Identify the preparation type.
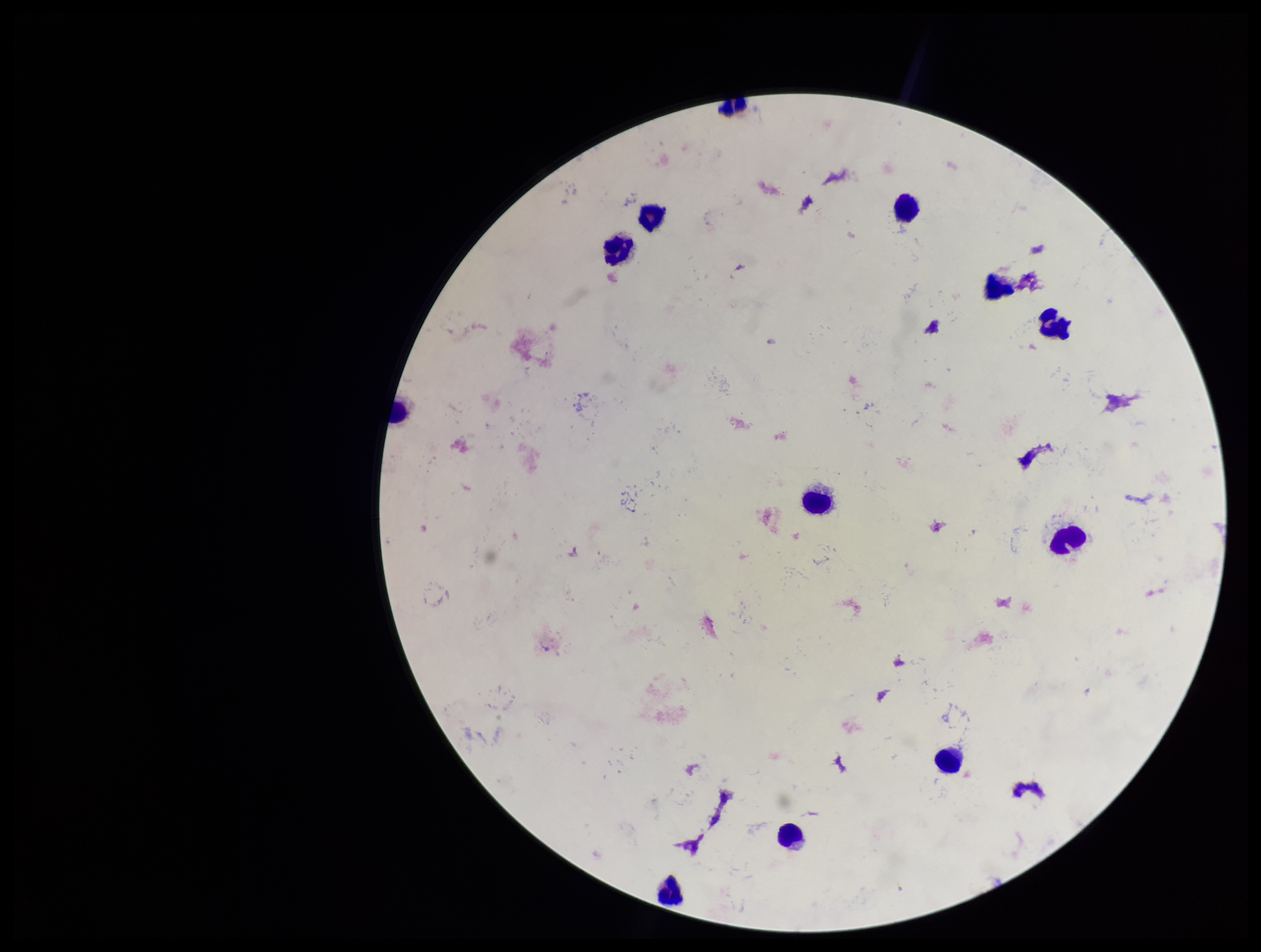

It is a thick blood smear.

parasite count = 0
stain = Giemsa
field of view = one from this slide
image size = 1261×952 pixels
patient malaria status = negative
Plasmodium parasites = none identified
leukocyte count = 12
capture = smartphone photograph through the microscope eyepiece